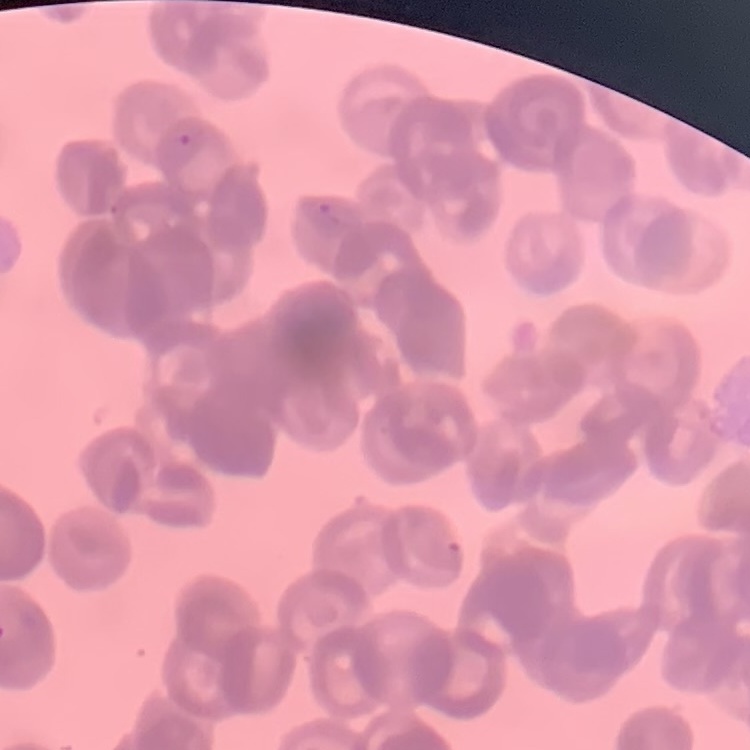

red blood cell morphology = rouleaux formation
preparation = thin blood smear
stain = Field's or Giemsa
image type = square crop of a larger photomicrograph